Locate every blood parasite and identify its species.
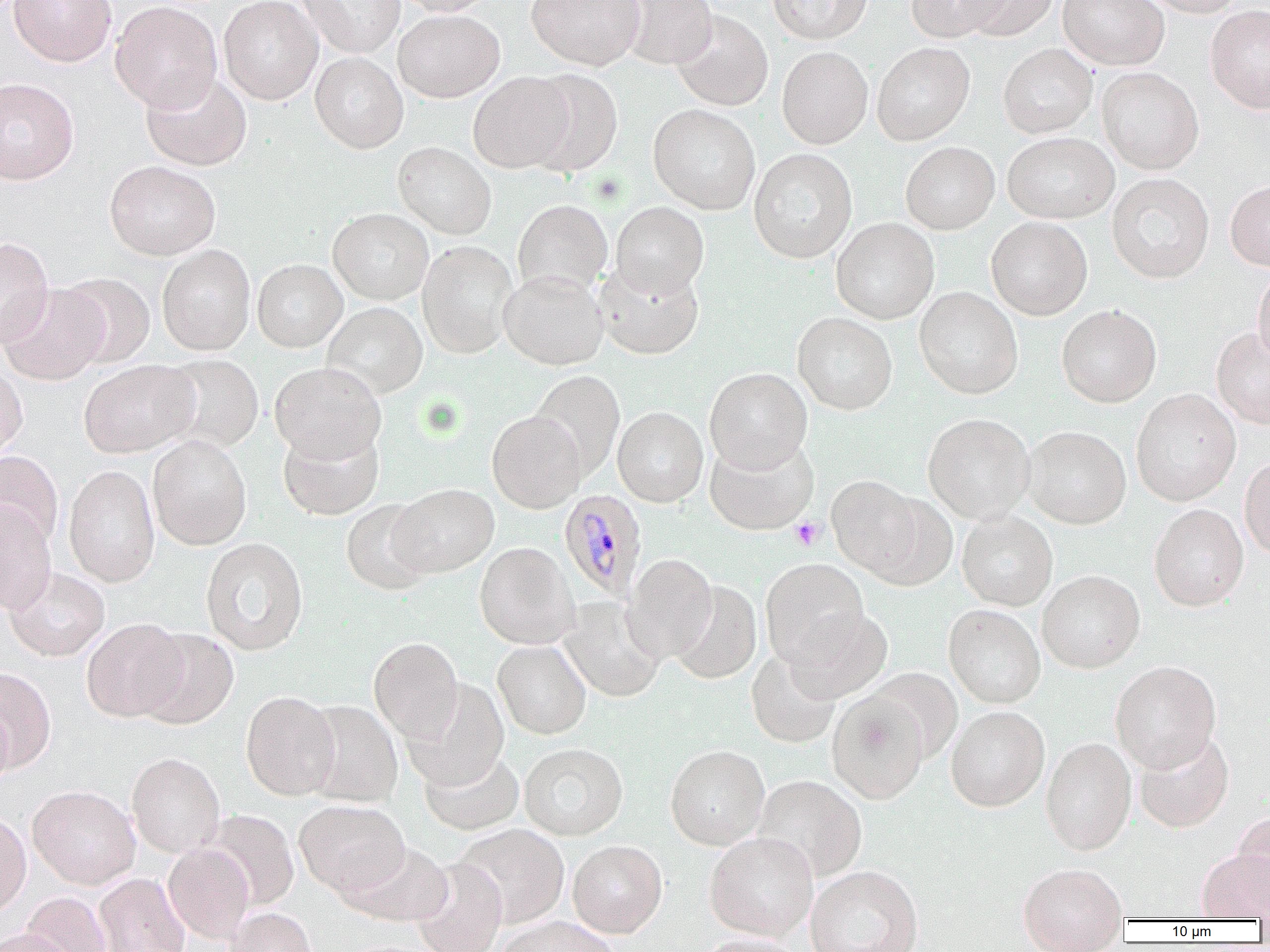
Approximate bounding boxes as (x1,y1)-(x2,y2) corner pairs in pixels.
Plasmodium malariae-infected red blood cells: (560,489)-(647,601).
No Plasmodium falciparum, Plasmodium ovale, Plasmodium vivax, Babesia divergens, or Trypanosoma brucei observed.

Platelet locations: (790,517)-(825,550). Uninfected red blood cell locations: (8,0)-(116,66), (218,0)-(323,105), (298,0)-(406,58), (395,0)-(498,16), (527,0)-(645,70), (616,0)-(718,69), (767,0)-(873,44), (905,0)-(1011,43), (958,0)-(1060,41), (1058,0)-(1169,69), (1139,0)-(1247,17), (110,1)-(222,113), (1205,6)-(1270,114), (393,9)-(505,102), (671,11)-(773,111), (872,41)-(975,146), (998,43)-(1097,138), (776,46)-(873,149), (310,52)-(408,153), (1097,67)-(1204,174), (524,68)-(624,177), (140,71)-(252,171), (468,72)-(574,173), (0,78)-(79,185), (648,104)-(760,214), (1003,132)-(1119,224), (393,141)-(497,240), (900,141)-(999,234), (749,148)-(857,263), (104,160)-(220,260), (1107,173)-(1215,283), (1225,179)-(1270,271), (513,199)-(613,296), (611,201)-(709,298), (328,208)-(434,305), (986,217)-(1093,320), (831,218)-(940,324), (0,236)-(54,349), (418,240)-(518,358), (157,244)-(256,355), (252,259)-(347,352), (593,261)-(705,359), (1252,267)-(1270,365), (499,269)-(608,370), (57,272)-(156,368), (0,283)-(109,385), (914,287)-(1023,399), (322,302)-(427,399), (1056,304)-(1162,407), (792,312)-(898,415), (1211,326)-(1270,430), (158,354)-(265,454), (79,360)-(199,458), (269,361)-(387,462), (0,364)-(28,459), (704,367)-(813,473), (530,370)-(625,481), (1131,388)-(1241,506), (613,406)-(708,507), (487,410)-(586,513), (922,413)-(1034,524), (278,425)-(384,520), (1021,425)-(1131,528), (147,435)-(251,550), (705,437)-(818,535), (0,451)-(64,549), (1239,456)-(1270,561), (63,465)-(161,587), (827,475)-(927,581), (388,483)-(499,578), (865,492)-(959,591), (340,498)-(438,596), (0,502)-(57,615), (1149,504)-(1249,611), (957,511)-(1058,611), (200,537)-(309,655), (475,542)-(579,649), (622,553)-(719,663), (760,558)-(869,668), (5,567)-(109,661), (1037,571)-(1145,673), (670,581)-(762,684), (558,597)-(665,702), (943,605)-(1045,709), (783,609)-(893,704), (81,618)-(189,722), (134,628)-(240,729), (368,637)-(464,743), (493,640)-(591,739), (746,648)-(841,748), (1110,661)-(1221,773), (1,666)-(56,772), (866,668)-(963,763), (403,679)-(509,791), (241,691)-(341,800), (827,693)-(929,804), (303,700)-(403,807), (0,701)-(14,792), (946,707)-(1050,812), (1135,731)-(1234,833), (1041,738)-(1136,856), (519,743)-(628,840), (665,746)-(770,849), (419,749)-(525,836), (127,752)-(225,858), (753,775)-(868,882), (27,784)-(141,889), (295,799)-(409,898), (203,809)-(299,910), (0,810)-(31,919), (1232,812)-(1270,910), (454,823)-(570,928), (704,832)-(818,940), (567,840)-(667,938), (163,842)-(255,944), (344,842)-(454,926), (1198,849)-(1270,920), (411,858)-(507,952), (1017,864)-(1128,949), (805,865)-(924,952), (93,873)-(190,952), (21,892)-(111,952), (224,907)-(317,952), (493,916)-(619,952), (0,928)-(78,952), (696,934)-(808,952). Slide-level diagnosis: Plasmodium malariae. Image is 1270×952 pixels. 1000x magnification. Thin blood smear. Optical microscopy. Single field of view.